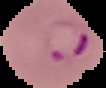

Summary:
  - Preparation: thin blood film
  - Image type: segmented cell region on a black background
  - Image size: 106×88 pixels
  - Malaria status: parasitized